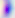

Photomicrograph. Toxoplasma gondii is seen. Captured at 400x magnification.